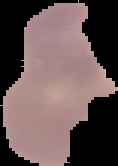 From a thin blood film. Image is 118×166 pixels. Malaria status: parasitized. Segmented cell region on a black background.